Assess this cell for malaria.
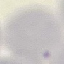
It is uninfected.

Summary:
  - Capture: smartphone camera at the microscope eyepiece
  - Preparation: thin blood smear
  - Image type: cell patch, automatically extracted from a larger field of view and resized to 64 × 64 pixels
  - Stain: Giemsa